Report the malaria status of this cell.
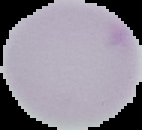
It is uninfected.

image_type: segmented cell region with the area outside set to black
image_size: 142×130 pixels
preparation: thin blood smear